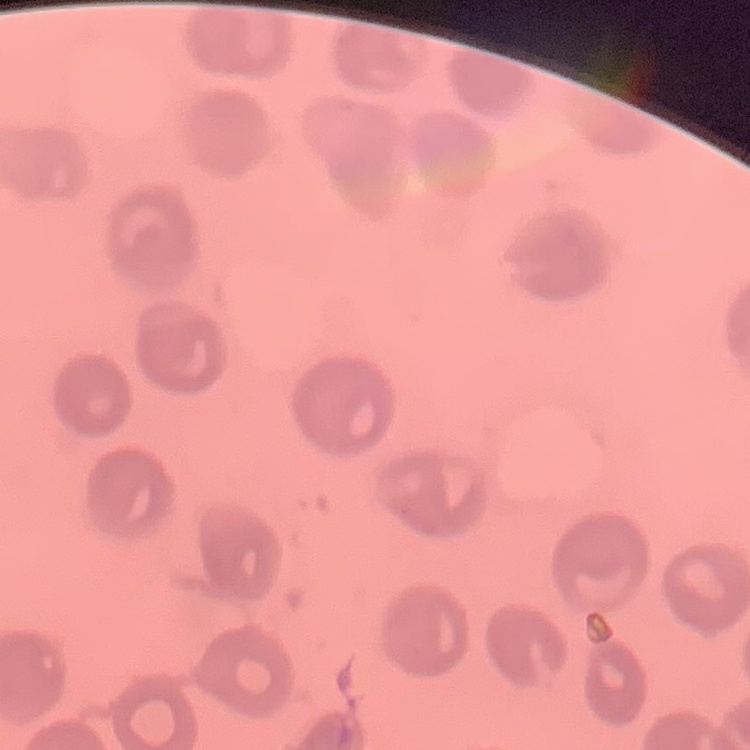

{
  "erythrocyte_morphology": "no rouleaux formation",
  "stain": "Field's or Giemsa",
  "image_type": "square crop of a larger photomicrograph",
  "preparation": "thin blood smear"
}